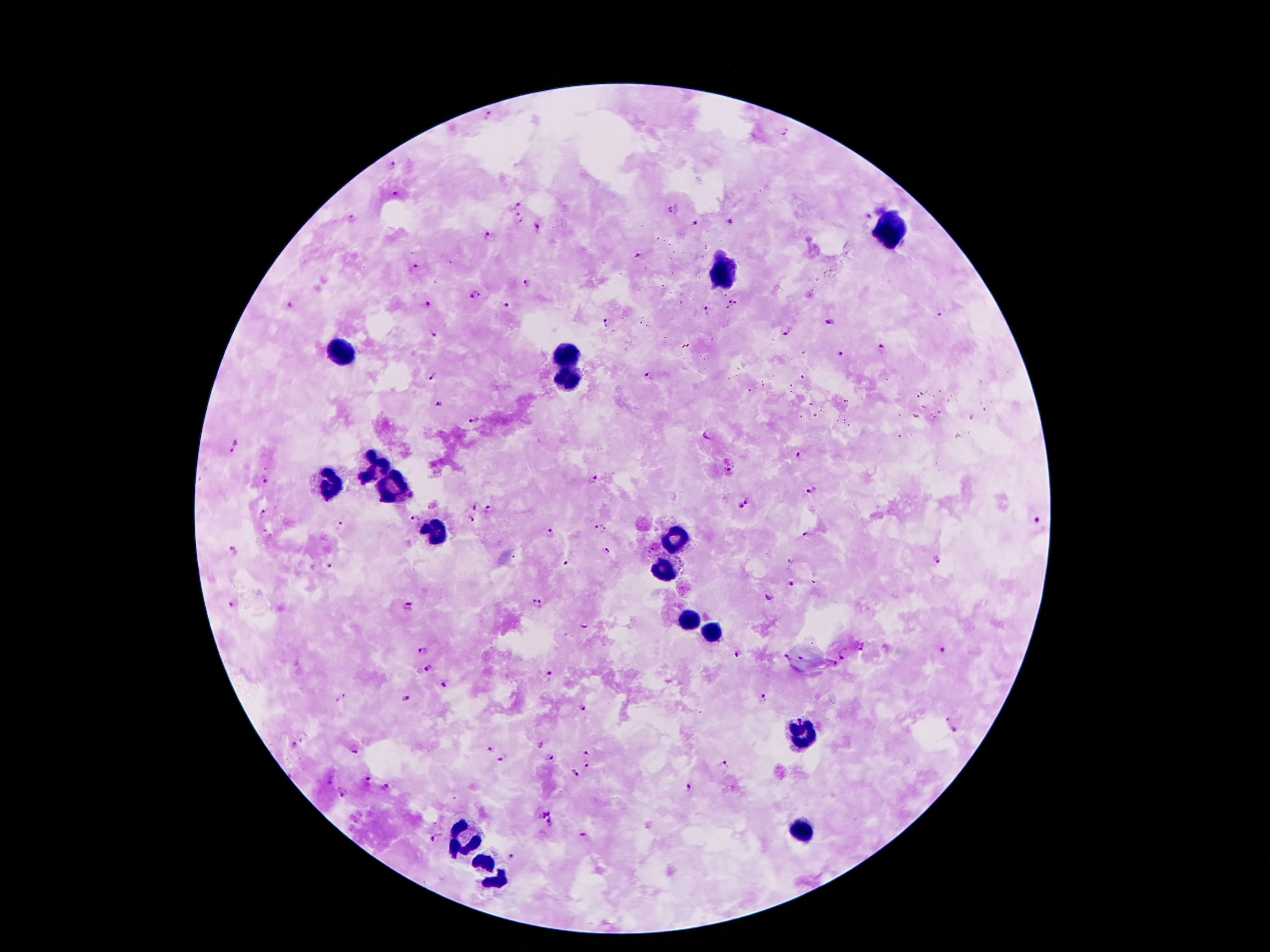

Approximate centers as {x, y} in pixels.
Summary:
  - Malaria parasite locations: {488, 114}, {782, 131}, {392, 162}, {394, 193}, {517, 205}, {673, 209}, {516, 215}, {352, 219}, {521, 221}, {732, 221}, {695, 223}, {538, 227}, {490, 236}, {640, 255}, {415, 265}, {526, 281}, {474, 292}, {429, 302}, {734, 302}, {508, 305}, {288, 306}, {706, 311}, {942, 311}, {607, 321}, {831, 323}, {784, 331}, {435, 332}, {884, 350}, {840, 353}, {650, 374}, {430, 377}, {438, 403}, {473, 420}, {706, 436}, {235, 446}, {799, 456}, {729, 469}, {266, 480}, {592, 480}, {811, 491}, {748, 500}, {475, 505}, {739, 507}, {490, 510}, {265, 513}, {414, 519}, {472, 520}, {1039, 521}, {340, 525}, {601, 528}, {551, 533}, {807, 533}, {233, 551}, {608, 552}, {937, 559}, {791, 561}, {568, 563}, {328, 565}, {792, 584}, {769, 597}, {233, 603}, {538, 603}, {408, 607}, {585, 626}, {863, 646}, {942, 650}, {423, 651}, {738, 654}, {843, 655}, {786, 657}, {835, 664}, {431, 668}, {550, 673}, {446, 685}, {341, 697}, {765, 697}, {408, 698}, {583, 708}, {948, 719}, {955, 730}, {540, 744}, {295, 745}, {355, 748}, {489, 749}, {587, 753}, {502, 757}, {550, 757}, {724, 765}, {587, 768}, {573, 773}, {330, 777}, {367, 779}, {385, 787}, {690, 787}, {343, 793}, {547, 817}, {584, 836}, {434, 837}, {512, 855}
  - Leukocyte locations: {887, 232}, {721, 276}, {337, 356}, {566, 356}, {566, 379}, {375, 465}, {333, 486}, {391, 486}, {433, 530}, {679, 530}, {664, 568}, {685, 621}, {708, 635}, {801, 734}, {803, 831}, {463, 835}, {490, 871}
  - Image size: 1270×952 pixels
  - Patient malaria status: infected with Plasmodium falciparum
  - Preparation: thick blood film
  - Capture: smartphone camera through the microscope eyepiece
  - Magnification: 100x
  - Field of view: single
  - Stain: Giemsa